State which parasite is depicted.
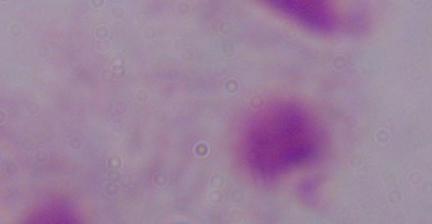
A trichomonad.

1000x magnification. Micrograph.